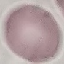
result: no malaria parasites seen
image_type: automatically extracted cell patch, resized to 64 × 64 pixels
stain: Giemsa
preparation: thin blood smear
capture: smartphone through the microscope eyepiece